Locate every Plasmodium ovale-infected red blood cell.
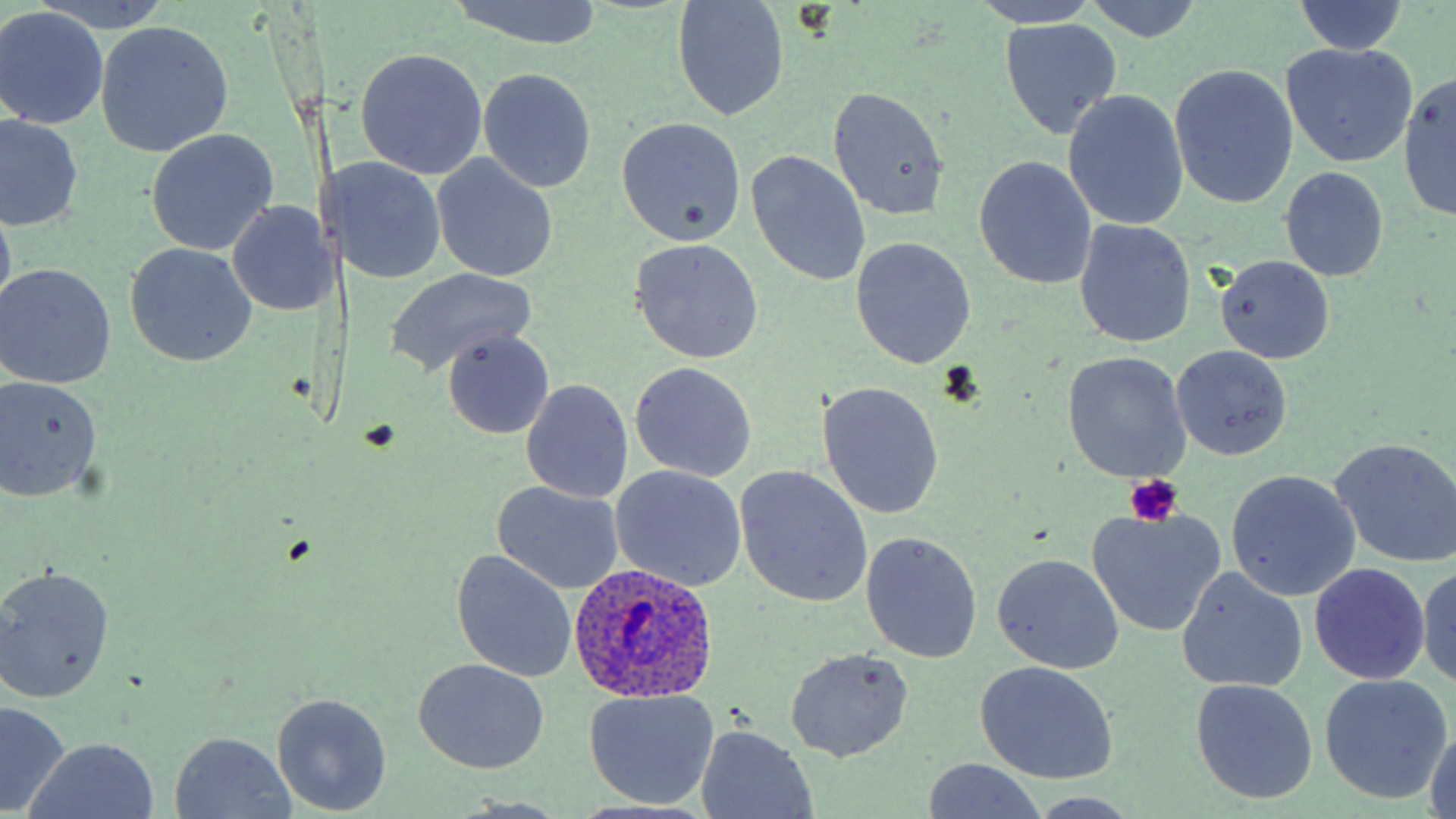
Approximate bounding boxes as (x1, y1, x2, y2) in pixels.
Plasmodium ovale-infected red blood cells: (567, 558, 721, 704).

Uninfected red blood cell locations: (443, 0, 604, 48), (670, 0, 792, 121), (1081, 0, 1208, 44), (969, 1, 1106, 29), (1290, 1, 1410, 56), (0, 8, 109, 130), (998, 18, 1121, 140), (96, 21, 233, 156), (1280, 44, 1417, 169), (354, 47, 488, 180), (1169, 64, 1298, 210), (476, 67, 596, 193), (1400, 72, 1456, 223), (828, 89, 949, 220), (1064, 93, 1189, 230), (0, 115, 83, 233), (615, 116, 747, 246), (146, 128, 278, 255), (746, 151, 870, 288), (329, 155, 448, 285), (431, 155, 558, 281), (974, 156, 1097, 290), (1279, 168, 1388, 282), (0, 194, 17, 321), (225, 199, 332, 315), (152, 216, 306, 347), (1075, 221, 1197, 349), (850, 238, 975, 368), (628, 239, 764, 363), (123, 242, 258, 367), (1215, 255, 1335, 363), (1, 264, 116, 389), (386, 268, 538, 374), (441, 331, 555, 437), (1170, 344, 1294, 461), (475, 350, 603, 480), (1062, 353, 1191, 482), (629, 362, 756, 482), (0, 376, 102, 503), (521, 379, 633, 504), (817, 382, 943, 520), (1329, 438, 1456, 567), (735, 465, 873, 608), (610, 466, 747, 591), (1227, 470, 1360, 602), (491, 482, 625, 594), (1088, 507, 1225, 637), (860, 532, 982, 663), (452, 548, 576, 682), (993, 554, 1123, 675), (1415, 561, 1456, 689), (1310, 563, 1431, 685), (0, 564, 117, 703), (1177, 567, 1308, 693), (785, 649, 914, 762), (412, 657, 550, 774), (975, 660, 1120, 784), (1319, 672, 1454, 804), (1193, 676, 1317, 804), (582, 689, 720, 809), (271, 693, 393, 815), (0, 702, 70, 816), (695, 728, 817, 817), (169, 732, 297, 816), (26, 737, 159, 819), (920, 762, 1052, 818). Platelet locations: (1121, 474, 1186, 526). Slide-level diagnosis: Plasmodium ovale. May-Grünwald-Giemsa stain. Light microscopy. Thin blood smear. Single field of view. Image is 1456×819 pixels. Captured at 1000x magnification.